Find each parasitized red blood cell.
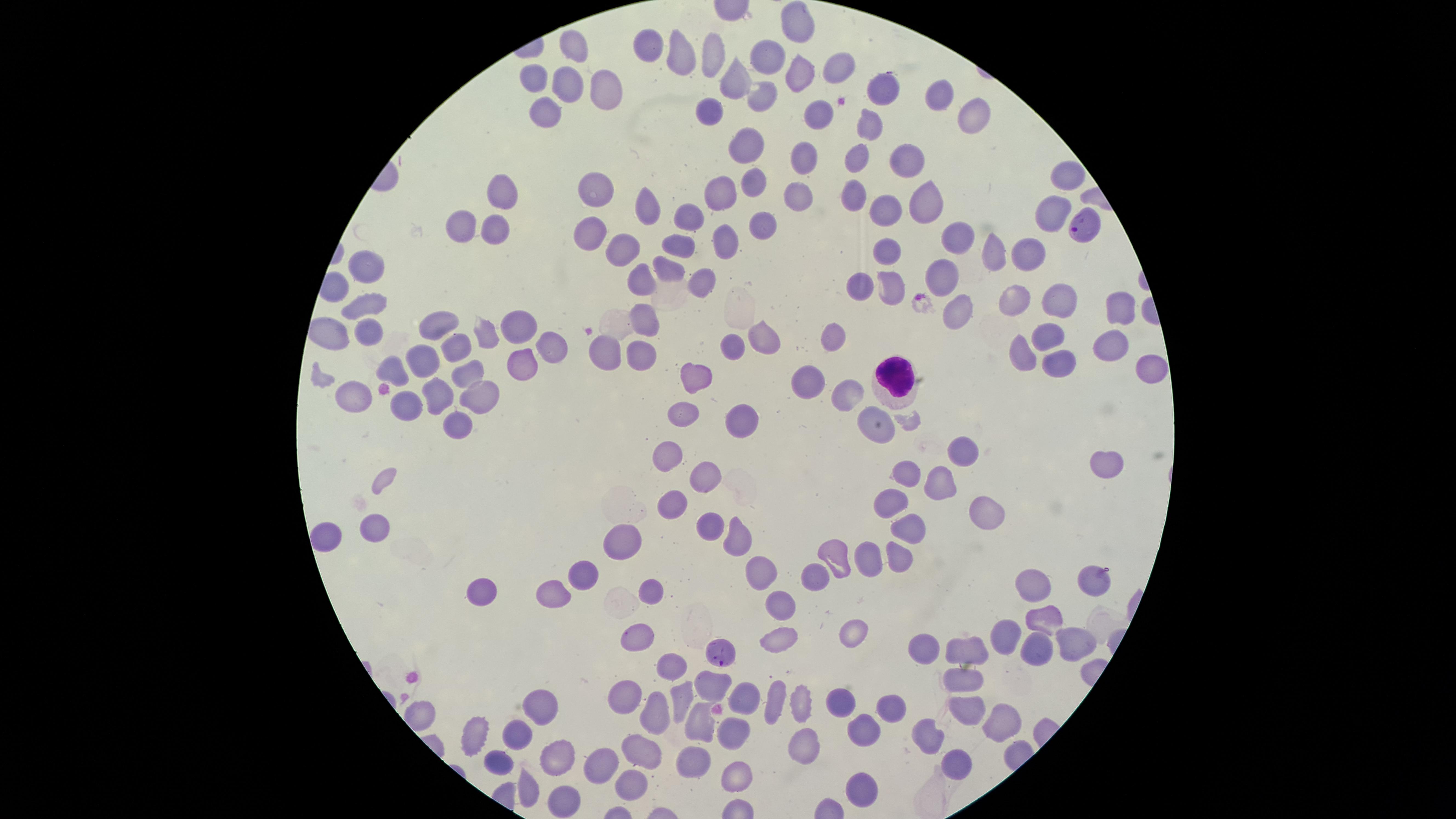

Approximate marker points as {x, y} in pixels.
Parasitized red blood cells: {1083, 223}, {723, 656}.

preparation: thin blood film
white_blood_cells: 'approximate marker points as {x, y} in pixels: {896, 376}'
uninfected_red_blood_cells: 'approximate marker points as {x, y} in pixels: {799, 26}, {655, 48}, {573, 53}, {678, 56}, {709, 58}, {766, 60}, {833, 66}, {797, 76}, {536, 81}, {733, 81}, {605, 83}, {568, 87}, {881, 87}, {761, 91}, {943, 94}, {544, 113}, {708, 115}, {815, 116}, {978, 119}, {867, 125}, {743, 143}, {804, 157}, {857, 159}, {905, 162}, {1065, 175}, {754, 180}, {591, 188}, {721, 191}, {794, 193}, {501, 195}, {852, 196}, {923, 198}, {651, 210}, {891, 211}, {1047, 211}, {686, 218}, {764, 218}, {461, 224}, {493, 227}, {728, 235}, {586, 236}, {953, 241}, {682, 249}, {617, 250}, {888, 250}, {992, 253}, {1025, 253}, {361, 269}, {669, 271}, {939, 274}, {643, 276}, {706, 280}, {863, 281}, {888, 286}, {1014, 295}, {1053, 300}, {1119, 308}, {362, 312}, {957, 313}, {445, 319}, {647, 321}, {326, 330}, {512, 330}, {1045, 333}, {829, 335}, {364, 337}, {481, 337}, {1107, 337}, {732, 345}, {765, 345}, {456, 346}, {555, 346}, {644, 350}, {606, 353}, {1063, 356}, {1024, 357}, {421, 362}, {390, 366}, {1150, 368}, {517, 373}, {464, 375}, {803, 376}, {701, 380}, {434, 387}, {844, 393}, {481, 394}, {346, 398}, {405, 406}, {685, 412}, {738, 415}, {453, 419}, {876, 429}, {958, 451}, {667, 459}, {1105, 460}, {707, 472}, {902, 472}, {936, 482}, {890, 501}, {675, 506}, {987, 515}, {711, 525}, {376, 528}, {906, 532}, {328, 538}, {733, 540}, {626, 541}, {831, 557}, {863, 558}, {894, 558}, {761, 571}, {585, 573}, {1098, 578}, {812, 579}, {1035, 587}, {650, 592}, {557, 594}, {485, 595}, {781, 603}, {1051, 616}, {854, 632}, {643, 633}, {1006, 636}, {782, 639}, {1069, 646}, {922, 648}, {974, 650}, {1034, 652}, {671, 663}, {965, 678}, {710, 680}, {627, 694}, {684, 695}, {748, 695}, {774, 697}, {843, 701}, {800, 705}, {892, 706}, {535, 709}, {969, 709}, {653, 712}, {703, 718}, {1001, 723}, {865, 728}, {472, 730}, {728, 730}, {932, 730}, {516, 733}, {807, 741}, {641, 745}, {501, 757}, {958, 758}, {557, 759}, {698, 761}, {600, 764}, {742, 773}, {529, 787}, {631, 787}, {854, 792}, {568, 800}'
field_of_view: single
stain: Giemsa
capture: smartphone photograph through the microscope eyepiece
species: Plasmodium falciparum
image_size: 1456×819 pixels
visible_region: circular